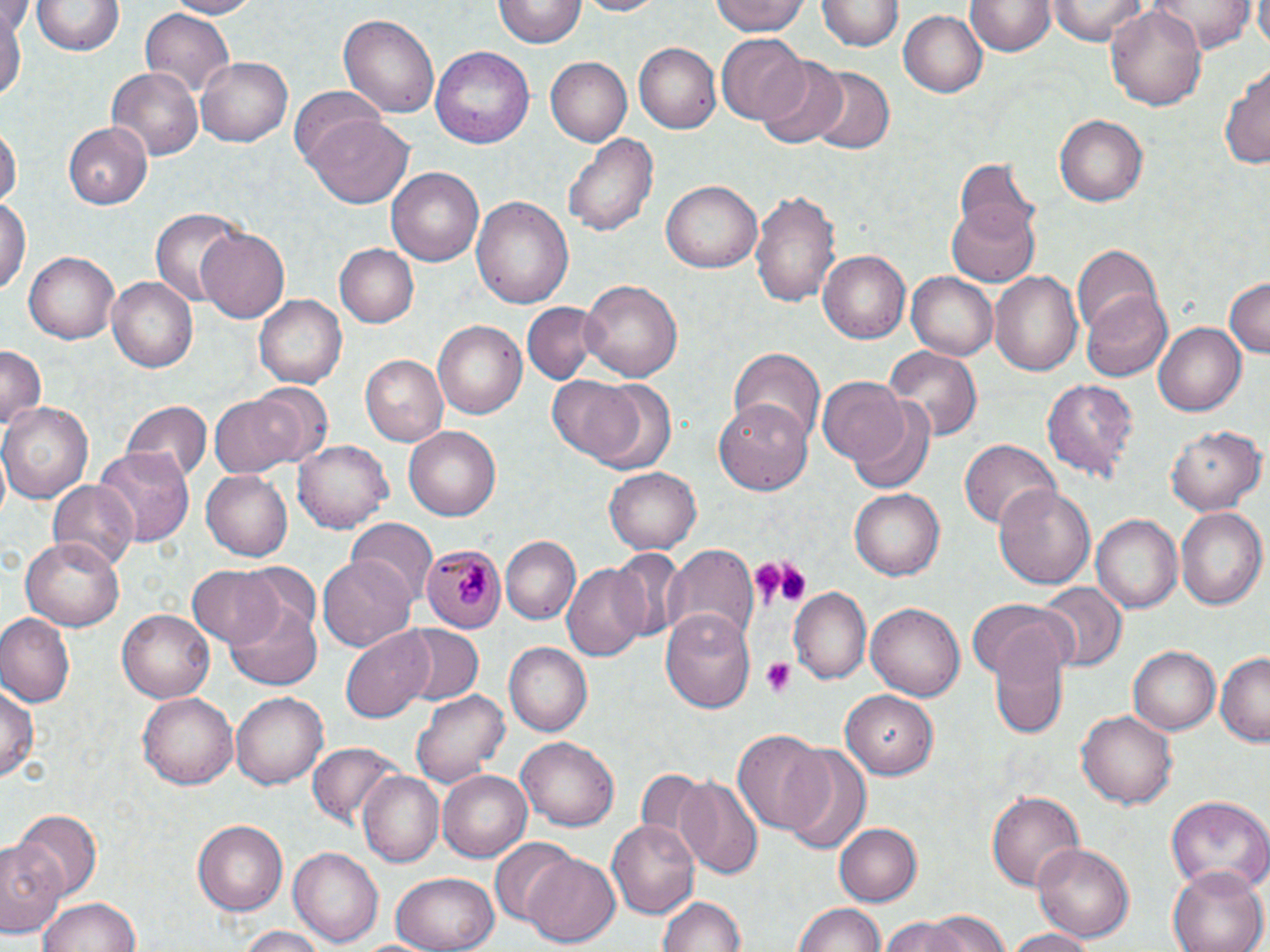

{
  "slide_level_diagnosis": "Plasmodium malariae",
  "magnification": "1000x",
  "preparation": "thin blood film",
  "modality": "optical microscopy",
  "image_size": "1270×952 pixels",
  "plasmodium_malariae_infected_red_blood_cell_locations": "approximate bounding boxes as [x1, y1, x2, y2] in pixels: [420, 544, 508, 635]",
  "field_of_view": "single",
  "stain": "May-Grünwald-Giemsa",
  "platelet_locations": "approximate bounding boxes as [x1, y1, x2, y2] in pixels: [748, 559, 807, 610], [760, 657, 798, 698]",
  "uninfected_red_blood_cell_locations": "approximate bounding boxes as [x1, y1, x2, y2] in pixels: [164, 0, 261, 18], [575, 0, 670, 17], [711, 0, 809, 36], [1046, 0, 1150, 45], [1147, 0, 1259, 53], [1253, 0, 1270, 49], [34, 1, 121, 57], [967, 1, 1054, 58], [493, 2, 584, 49], [818, 2, 901, 52], [1106, 4, 1210, 113], [0, 6, 24, 109], [138, 9, 236, 103], [901, 9, 987, 98], [338, 12, 440, 117], [716, 35, 808, 125], [633, 43, 719, 133], [430, 45, 535, 148], [547, 56, 633, 146], [198, 57, 292, 146], [758, 57, 848, 147], [1218, 61, 1270, 169], [104, 66, 204, 161], [804, 67, 894, 155], [292, 87, 389, 178], [1055, 114, 1149, 207], [307, 119, 413, 208], [64, 121, 153, 209], [0, 126, 19, 214], [563, 130, 657, 239], [953, 159, 1040, 246], [388, 167, 484, 267], [661, 179, 763, 272], [751, 189, 839, 307], [0, 192, 29, 302], [472, 197, 574, 308], [946, 199, 1041, 285], [150, 208, 249, 308], [197, 228, 290, 325], [1071, 242, 1163, 338], [333, 243, 417, 328], [817, 249, 911, 344], [23, 251, 119, 345], [990, 269, 1083, 377], [906, 270, 998, 360], [1223, 276, 1269, 359], [107, 277, 198, 373], [578, 278, 684, 385], [1083, 290, 1171, 382], [257, 294, 346, 388], [522, 302, 601, 382], [1155, 320, 1246, 417], [432, 321, 527, 420], [0, 345, 45, 439], [881, 345, 981, 444], [726, 347, 824, 442], [358, 355, 447, 447], [1041, 375, 1138, 482], [548, 376, 666, 470], [817, 378, 910, 469], [245, 384, 332, 463], [209, 391, 306, 479], [713, 399, 815, 493], [121, 400, 210, 485], [852, 400, 937, 494], [2, 401, 92, 502], [1167, 423, 1264, 515], [404, 426, 500, 520], [293, 439, 390, 534], [959, 440, 1058, 529], [93, 445, 194, 547], [605, 468, 701, 555], [201, 470, 293, 561], [48, 480, 138, 570], [993, 482, 1096, 591], [849, 488, 943, 580], [1175, 505, 1268, 611], [1090, 514, 1183, 615], [346, 519, 434, 607], [500, 536, 579, 624], [21, 537, 125, 632], [659, 544, 759, 653], [607, 547, 686, 644], [319, 558, 418, 651], [562, 561, 652, 660], [187, 564, 285, 648], [1039, 582, 1126, 671], [790, 589, 871, 683], [229, 595, 323, 689], [866, 599, 966, 697], [969, 602, 1075, 688], [661, 608, 755, 716], [117, 609, 215, 702], [0, 613, 76, 707], [394, 624, 485, 705], [987, 625, 1070, 737], [341, 629, 436, 722], [504, 644, 590, 736], [1128, 645, 1223, 735], [1215, 653, 1269, 744], [1, 682, 38, 784], [842, 688, 941, 777], [411, 689, 508, 787], [138, 692, 240, 791], [231, 692, 327, 788], [1077, 710, 1180, 810], [733, 728, 831, 836], [516, 734, 621, 831], [309, 742, 400, 829], [780, 744, 872, 853], [633, 766, 713, 859], [437, 771, 531, 862], [359, 772, 444, 868], [677, 777, 764, 881], [986, 789, 1085, 892], [1164, 794, 1270, 893], [12, 810, 101, 902], [193, 820, 288, 914], [607, 822, 698, 914], [835, 822, 923, 907], [0, 836, 64, 937], [489, 838, 577, 926], [1032, 840, 1136, 944], [291, 847, 382, 948], [523, 854, 621, 948], [1168, 865, 1268, 952], [389, 871, 499, 952], [37, 895, 142, 952], [657, 896, 749, 952], [795, 902, 888, 952], [926, 912, 1010, 952], [877, 919, 983, 952], [231, 926, 335, 952], [1003, 927, 1096, 952]"
}